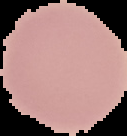

The area outside the segmented cell region is set to black. Image is 127×136 pixels. From a thin blood film. Malaria status: uninfected.